Report the malaria status of this cell.
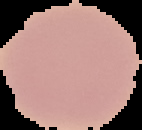

Uninfected.

Image is 142×130 pixels. Cell region segmented out of the field of view; the surrounding area is masked to black. From a thin blood film.